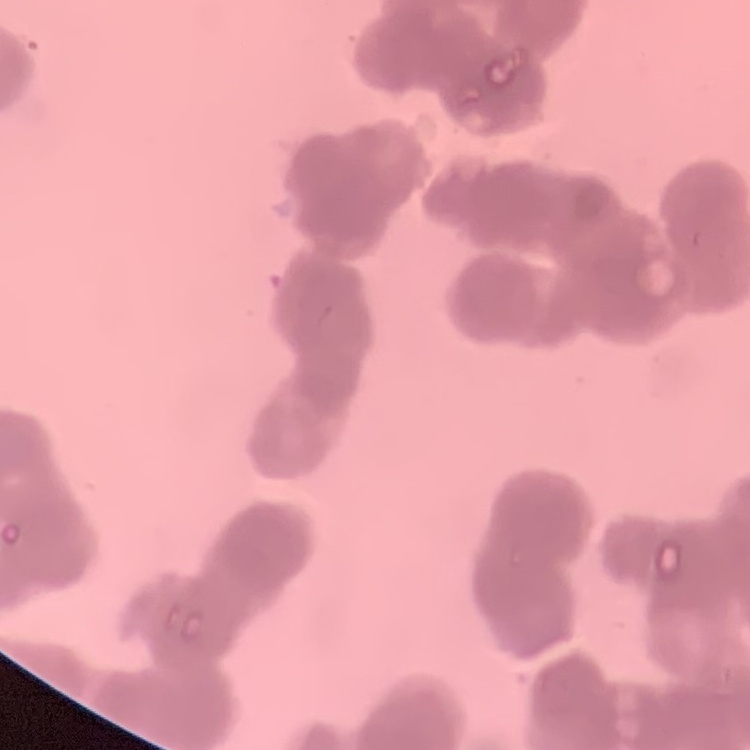

The red blood cells show rouleaux formation. Thin blood film. Square crop of a larger photomicrograph. Stained with either Field's or Giemsa.